Classify this cell by malaria status.
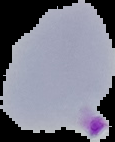
Parasitized.

Summary:
  - Image type: cell region segmented out of the field of view; surrounding area masked to black
  - Preparation: thin blood smear
  - Image size: 115×142 pixels